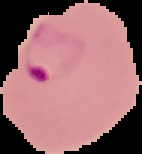
Image is 142×154 pixels. Segmented cell region on a black background. Result: Plasmodium parasites detected. From a thin blood film.